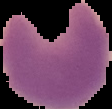

image type = segmented cell region on a black background
image size = 112×109 pixels
malaria status = parasitized
preparation = thin blood film